Assess this cell for malaria.
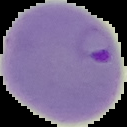
Parasitized.

image_type: segmented cell region on a black background
image_size: 127×127 pixels
preparation: thin blood film